Comment on the morphology of the erythrocytes.
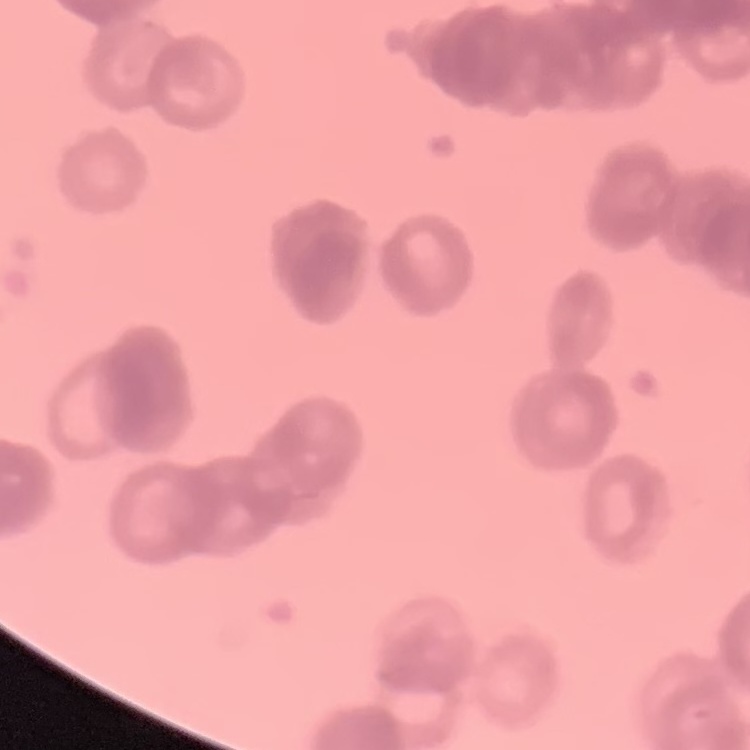
They show rouleaux formation.

Summary:
  - Preparation: thin peripheral smear
  - Image type: square crop of a larger photomicrograph
  - Stain: Field's or Giemsa